Locate every uninfected red blood cell.
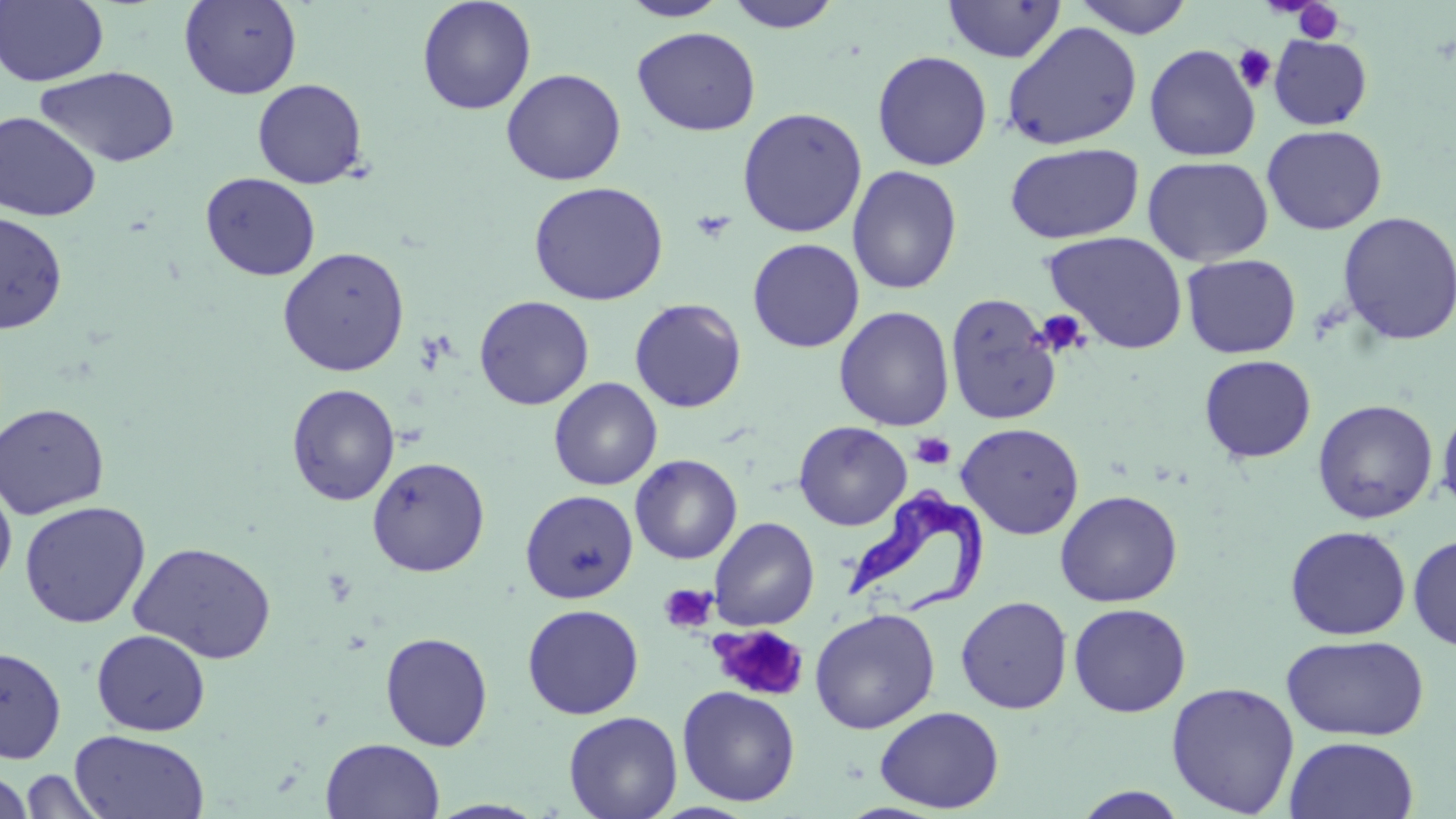
Approximate bounding boxes as [x1, y1, x2, y2] in pixels.
Uninfected red blood cells: [0, 0, 108, 87], [179, 0, 303, 99], [416, 0, 537, 115], [617, 0, 731, 21], [1072, 0, 1195, 39], [723, 1, 844, 32], [942, 1, 1067, 63], [1001, 22, 1143, 150], [632, 27, 761, 136], [1268, 34, 1373, 130], [1144, 44, 1261, 162], [872, 50, 993, 171], [35, 66, 180, 168], [501, 68, 626, 186], [252, 78, 368, 189], [737, 106, 868, 238], [0, 111, 101, 222], [1262, 124, 1387, 235], [1004, 142, 1144, 244], [1142, 155, 1274, 266], [846, 165, 963, 295], [200, 172, 321, 281], [528, 181, 669, 306], [0, 211, 68, 333], [1335, 212, 1455, 346], [1045, 231, 1188, 354], [747, 238, 865, 353], [277, 246, 410, 377], [1181, 253, 1301, 359], [945, 292, 1063, 424], [474, 295, 594, 410], [629, 298, 746, 413], [834, 306, 955, 431], [1198, 354, 1317, 463], [549, 377, 662, 491], [286, 383, 401, 506], [1313, 399, 1438, 523], [1437, 400, 1456, 519], [0, 403, 110, 519], [793, 421, 912, 530], [956, 422, 1084, 539], [629, 454, 742, 564], [367, 456, 490, 577], [0, 476, 17, 593], [1055, 489, 1182, 607], [521, 490, 638, 603], [19, 500, 151, 629], [709, 517, 820, 631], [1285, 525, 1411, 640], [1408, 533, 1456, 652], [128, 540, 278, 664], [955, 595, 1073, 714], [1068, 602, 1191, 717], [522, 604, 644, 719], [810, 608, 940, 734], [91, 629, 211, 736], [379, 632, 493, 751], [1280, 634, 1430, 742], [0, 646, 67, 764], [1166, 681, 1300, 817], [677, 686, 800, 807], [874, 706, 1005, 813], [563, 711, 683, 819], [70, 729, 211, 818], [1285, 735, 1419, 819], [321, 737, 445, 819], [17, 768, 110, 818], [0, 771, 35, 818], [1072, 786, 1190, 818], [427, 799, 548, 818].

Trypanosoma brucei locations: [845, 489, 991, 621]. Platelet locations: [1292, 1, 1345, 44], [1233, 43, 1277, 93], [691, 209, 737, 243], [1036, 309, 1090, 358], [911, 432, 954, 470], [658, 583, 718, 633], [710, 625, 809, 703]. Slide-level diagnosis: Trypanosoma brucei. One field of a larger specimen. 1000x magnification. May-Grünwald-Giemsa-stained preparation. Thin blood smear. Optical microscopy. Image is 1456×819 pixels.